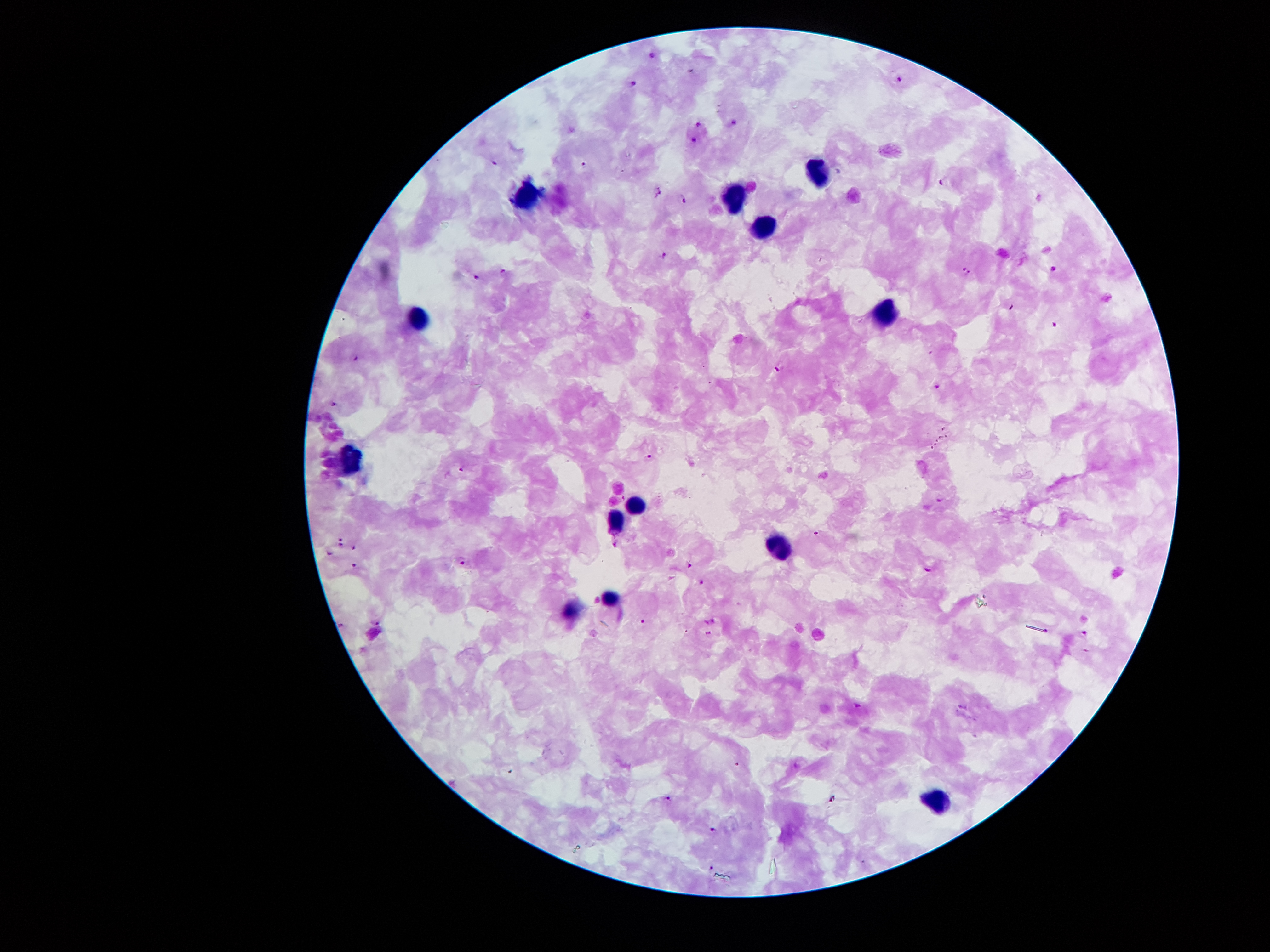
coordinate format = approximate centers as [x, y] in pixels
leukocyte locations = [816, 172], [524, 192], [739, 199], [763, 228], [886, 311], [420, 319], [348, 458], [638, 506], [613, 520], [781, 546], [610, 598], [571, 611], [940, 799]
Plasmodium parasite locations = [652, 55], [899, 80], [636, 85], [699, 123], [734, 123], [694, 142], [495, 160], [585, 167], [945, 181], [657, 191], [682, 198], [664, 256], [1055, 269], [967, 271], [501, 274], [476, 277], [1011, 308], [1055, 324], [355, 358], [780, 368], [939, 385], [335, 406], [649, 458], [464, 468], [942, 498], [342, 541], [616, 543], [355, 548], [330, 554], [463, 560], [691, 565], [355, 566], [928, 569], [703, 582], [642, 620], [377, 622], [342, 623], [706, 623], [708, 633], [1085, 633], [1086, 652], [857, 705], [669, 798], [712, 828], [712, 866]
image size = 1270×952 pixels
preparation = thick blood smear
stain = Giemsa
field of view = one from this slide
magnification = 100x
patient malaria status = infected with Plasmodium falciparum
capture = smartphone through the microscope eyepiece